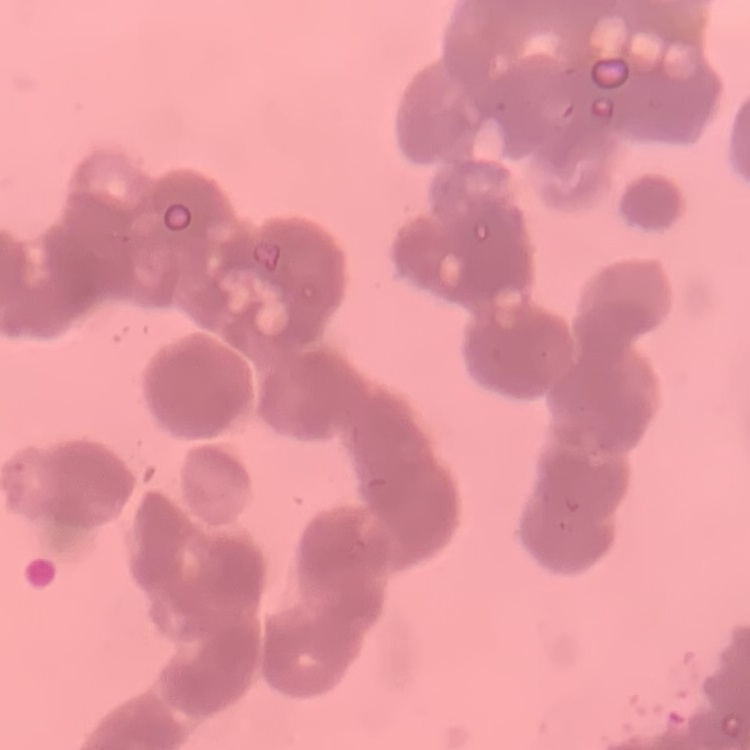
erythrocyte morphology = rouleaux formation
image type = square crop of a larger photomicrograph
preparation = thin blood smear
stain = Field's or Giemsa